Assess the morphology of the red blood cells.
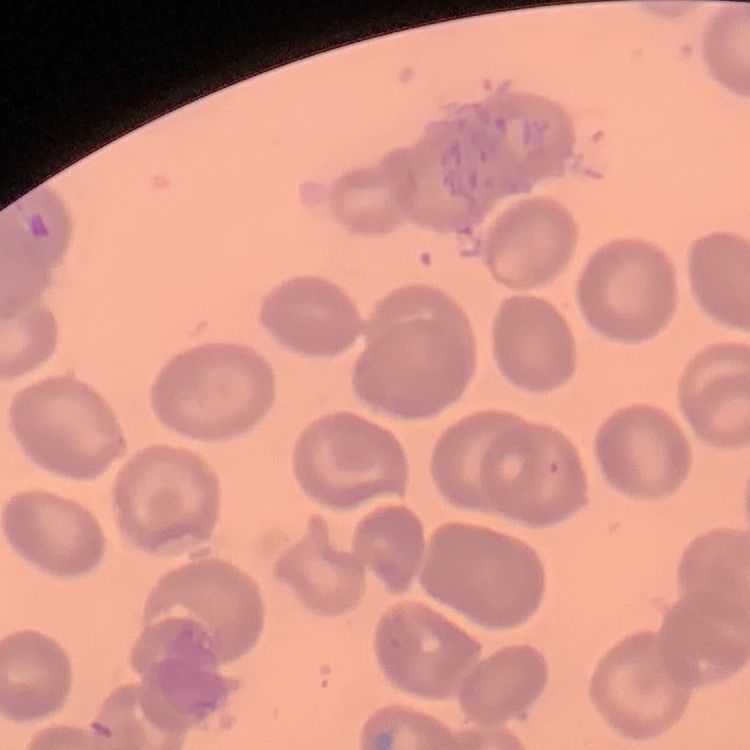

They show no rouleaux formation.

Stained with either Field's or Giemsa. Thin blood smear. One tile cut from a larger photomicrograph.